Describe the morphology of the erythrocytes.
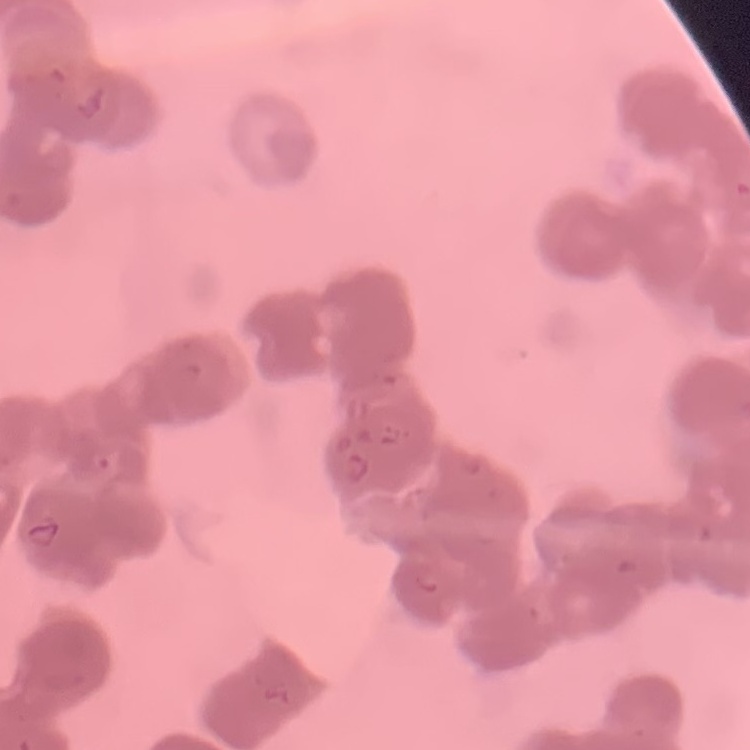
Rouleaux formation.

Summary:
  - Preparation: thin peripheral smear
  - Stain: Field's or Giemsa
  - Image type: square crop of a larger photomicrograph